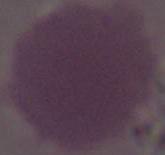
Summary:
  - Identification: erythrocyte
  - Magnification: 1000x
  - Modality: micrograph